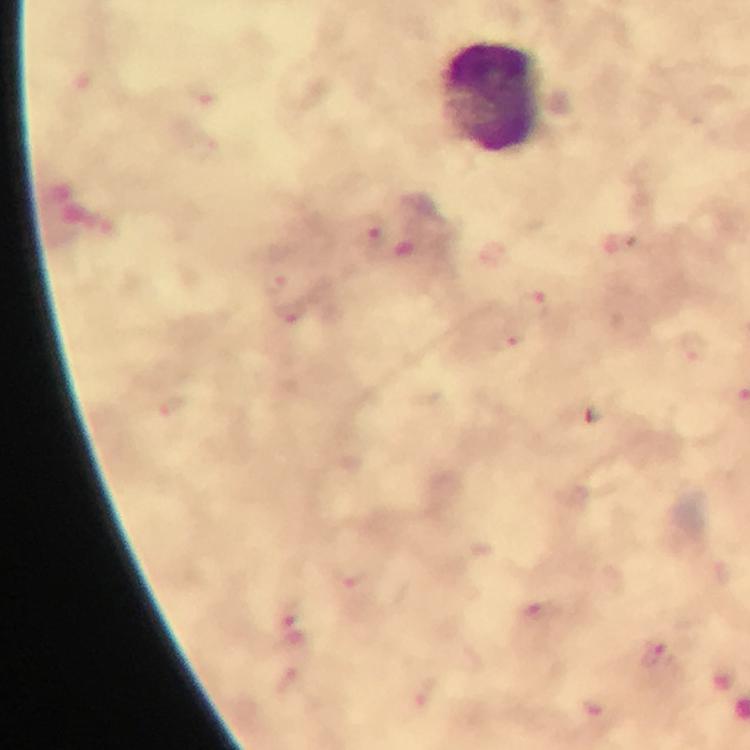
Approximate centers as (x, y) in pixels. Plasmodium parasite locations: (376, 232), (277, 283), (532, 299), (291, 314), (510, 339), (695, 348), (542, 609), (288, 627), (653, 654). Leukocyte locations: (494, 97). Image is 750×750 pixels. Giemsa stain. Thick blood smear. Immersion oil applied. Smartphone photograph taken through a microscope. 100x magnification. Cropped region of a single field of view. From a diagnostic examination for malaria.